Point out each malaria parasite.
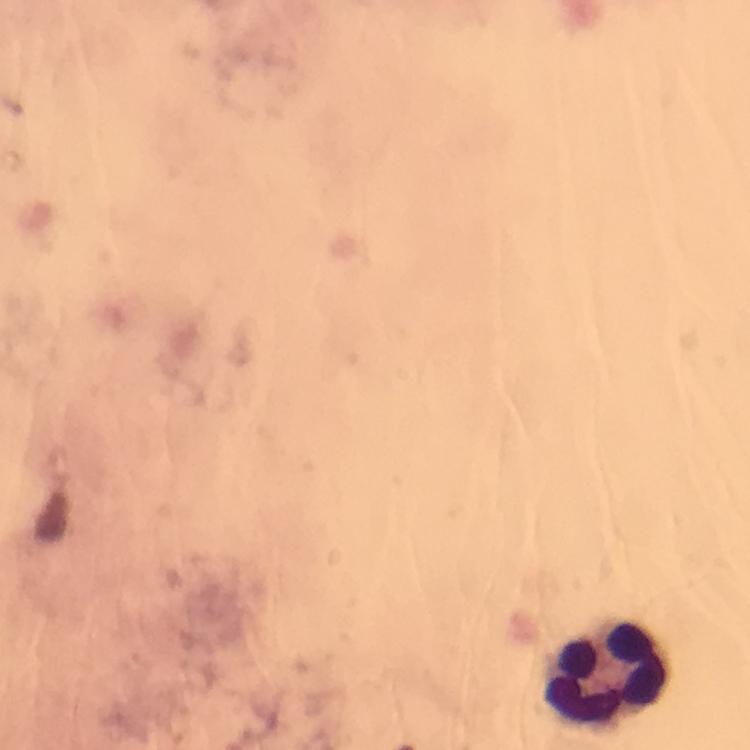
No malaria parasites detected.

Approximate centers as [x, y] in pixels.
Summary:
  - Leukocyte locations: [604, 674]
  - Image size: 750×750 pixels
  - Immersion oil: used
  - Capture: smartphone camera through the microscope
  - Preparation: thick blood film
  - Stain: Giemsa
  - Magnification: 100x
  - Context: from a malaria diagnostic workup
  - Cropped from: one field of view